Give the extent of all Plasmodium falciparum-infected red blood cells.
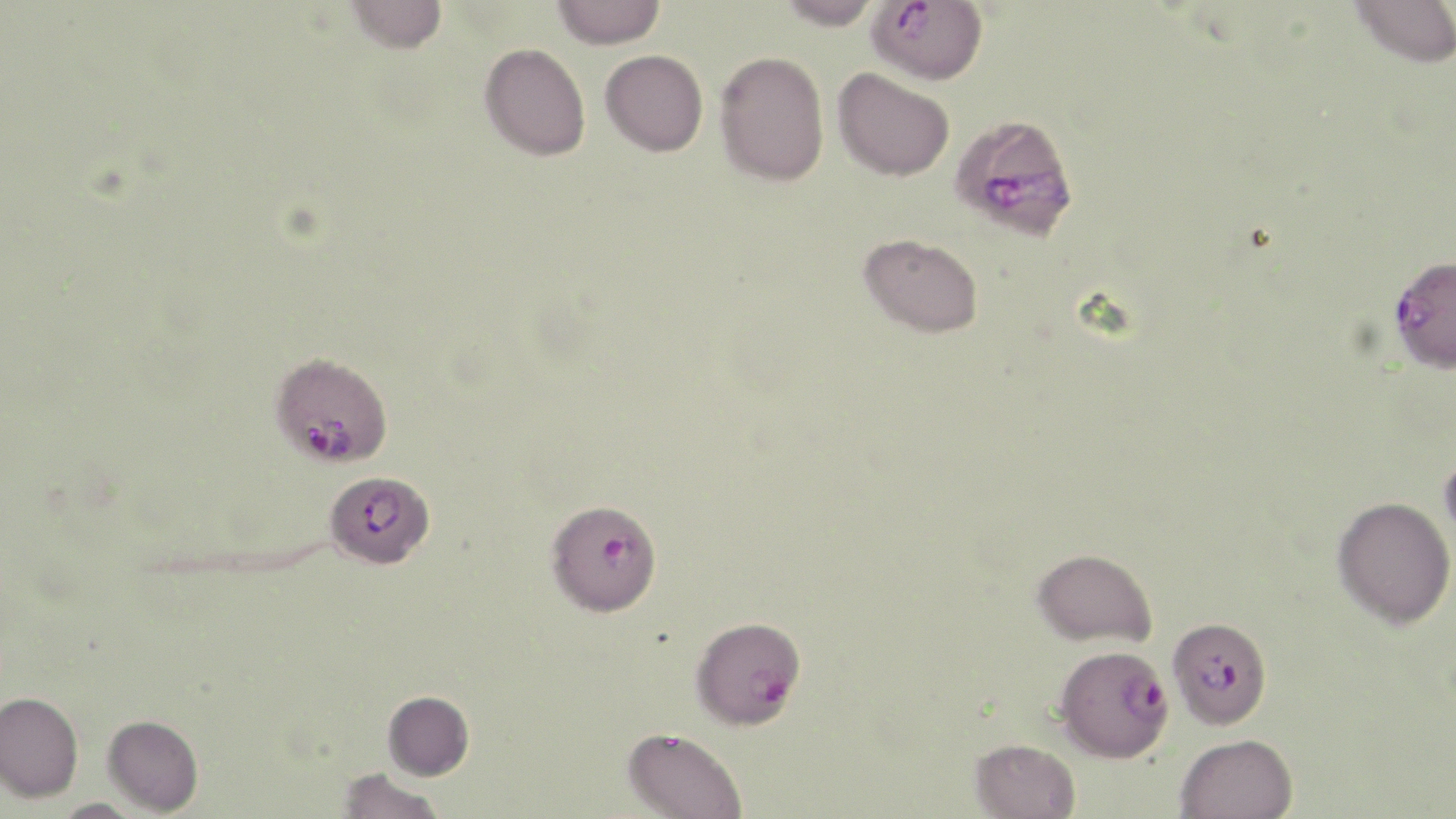

Approximate bounding boxes as named x1/y1/x2/y2 corners in pixels.
Plasmodium falciparum-infected red blood cells: (x1=866, y1=0, x2=988, y2=84), (x1=949, y1=113, x2=1080, y2=240), (x1=1388, y1=254, x2=1456, y2=373), (x1=271, y1=351, x2=393, y2=467), (x1=324, y1=470, x2=433, y2=569), (x1=548, y1=509, x2=662, y2=619), (x1=690, y1=616, x2=806, y2=730), (x1=1170, y1=623, x2=1268, y2=731), (x1=1054, y1=646, x2=1174, y2=762).

Uninfected red blood cell locations: (x1=344, y1=0, x2=448, y2=54), (x1=552, y1=0, x2=666, y2=49), (x1=776, y1=0, x2=883, y2=29), (x1=1349, y1=0, x2=1456, y2=68), (x1=479, y1=43, x2=591, y2=161), (x1=600, y1=49, x2=708, y2=156), (x1=715, y1=50, x2=829, y2=186), (x1=832, y1=67, x2=954, y2=181), (x1=859, y1=232, x2=983, y2=337), (x1=1439, y1=446, x2=1456, y2=548), (x1=1331, y1=496, x2=1455, y2=628), (x1=1031, y1=547, x2=1157, y2=646), (x1=383, y1=690, x2=474, y2=780), (x1=0, y1=691, x2=83, y2=802), (x1=103, y1=715, x2=203, y2=815), (x1=622, y1=727, x2=747, y2=819), (x1=1174, y1=733, x2=1298, y2=819), (x1=969, y1=738, x2=1080, y2=819), (x1=337, y1=768, x2=445, y2=819), (x1=51, y1=798, x2=145, y2=818). Slide-level diagnosis: Plasmodium falciparum. One field of a larger specimen. Optical microscopy. Image is 1456×819 pixels. Thin blood smear. May-Grünwald-Giemsa stain. 1000x magnification.